Identify the parasite.
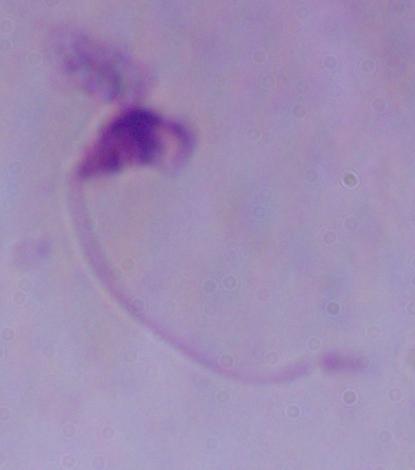
This is Leishmania.

{
  "magnification": "1000x",
  "modality": "micrograph"
}